Identify the blood parasite species.
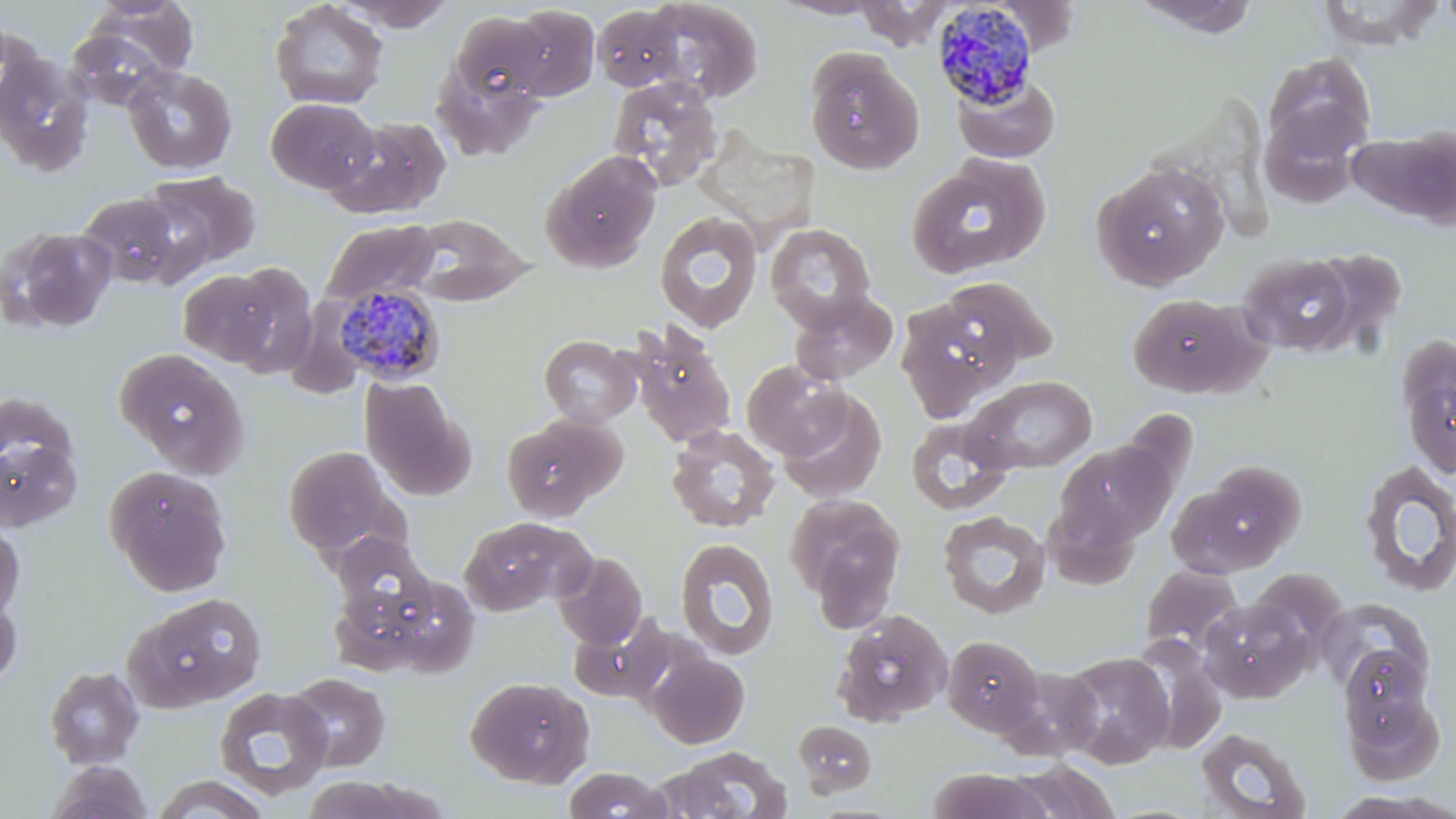
Plasmodium malariae.

modality = optical microscopy
image size = 1456×819 pixels
preparation = thin blood smear
magnification = 1000x
Plasmodium malariae-infected red blood cell locations = approximate bounding boxes as (x1, y1, x2, y2) in pixels: (930, 3, 1042, 110), (334, 285, 446, 384)
uninfected red blood cell locations = approximate bounding boxes as (x1, y1, x2, y2) in pixels: (642, 0, 764, 104), (767, 0, 887, 20), (1129, 0, 1263, 39), (1439, 0, 1456, 40), (86, 1, 200, 79), (269, 1, 389, 110), (335, 1, 457, 31), (855, 1, 958, 48), (1317, 1, 1441, 50), (504, 5, 600, 101), (592, 5, 687, 92), (451, 10, 552, 112), (63, 27, 174, 112), (0, 47, 96, 177), (804, 48, 924, 174), (431, 51, 548, 163), (1264, 52, 1376, 156), (123, 64, 237, 175), (951, 70, 1061, 164), (606, 75, 724, 192), (266, 97, 379, 194), (1259, 105, 1368, 208), (327, 115, 453, 218), (1350, 125, 1456, 228), (542, 150, 662, 273), (906, 155, 1051, 280), (1094, 162, 1230, 289), (140, 170, 262, 279), (76, 191, 185, 289), (654, 210, 764, 333), (404, 213, 532, 306), (320, 218, 440, 308), (765, 222, 878, 334), (1, 225, 117, 333), (1306, 247, 1408, 356), (1237, 252, 1359, 356), (221, 264, 317, 377), (179, 269, 281, 367), (937, 275, 1058, 375), (788, 289, 899, 385), (1127, 292, 1266, 399), (285, 297, 372, 398), (894, 298, 1012, 420), (629, 328, 737, 448), (539, 335, 641, 427), (1396, 337, 1456, 479), (114, 348, 250, 479), (742, 359, 850, 460), (963, 375, 1097, 474), (361, 378, 472, 501), (776, 389, 888, 505), (0, 392, 78, 483), (906, 415, 1015, 516), (501, 417, 617, 521), (665, 425, 780, 533), (0, 436, 82, 532), (1055, 438, 1176, 548), (282, 445, 408, 562), (1356, 462, 1456, 598), (1176, 464, 1304, 575), (103, 465, 232, 596), (784, 492, 906, 625), (938, 511, 1051, 620), (458, 516, 593, 616), (0, 522, 24, 624), (331, 534, 434, 626), (675, 538, 779, 660), (553, 552, 648, 649), (1139, 564, 1244, 659), (1245, 568, 1347, 670), (346, 572, 479, 678), (0, 590, 22, 688), (122, 592, 267, 714), (1200, 597, 1314, 702), (1317, 597, 1433, 700), (832, 609, 953, 727), (569, 615, 674, 704), (942, 635, 1044, 736), (1128, 635, 1227, 755), (1337, 647, 1435, 741), (647, 652, 749, 748), (1059, 652, 1175, 769), (44, 666, 145, 769), (996, 666, 1105, 761), (285, 672, 391, 772), (465, 675, 594, 788), (214, 686, 333, 801), (1343, 688, 1444, 784), (792, 720, 877, 796), (1194, 727, 1313, 819), (657, 746, 794, 819), (46, 761, 153, 819), (1003, 762, 1124, 818), (562, 767, 673, 818), (926, 769, 1054, 819), (150, 775, 272, 818), (301, 775, 443, 818)
stain = May-Grünwald-Giemsa
field of view = single